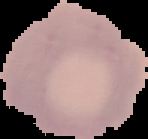 Segmented cell region on a black background. Image is 148×139 pixels. From a thin blood smear. Result: no Plasmodium parasites detected.